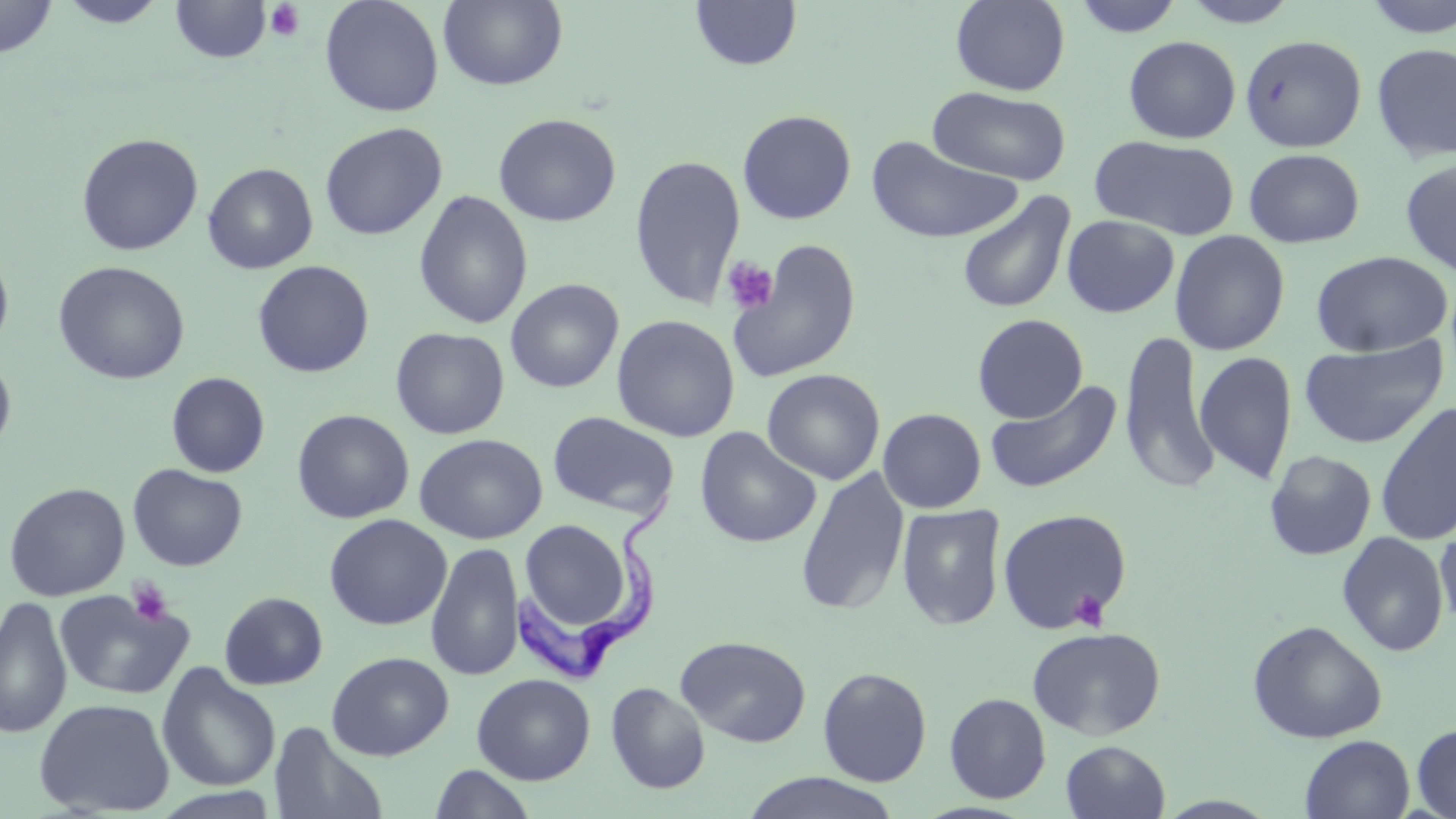 Approximate bounding boxes as named x1/y1/x2/y2 corners in pixels. Platelet locations: (x1=265, y1=2, x2=306, y2=43), (x1=721, y1=257, x2=780, y2=315), (x1=127, y1=578, x2=175, y2=627), (x1=1071, y1=590, x2=1109, y2=630). Trypanosoma brucei locations: (x1=513, y1=489, x2=677, y2=692). Uninfected red blood cell locations: (x1=0, y1=0, x2=57, y2=58), (x1=57, y1=0, x2=169, y2=28), (x1=320, y1=0, x2=444, y2=117), (x1=438, y1=0, x2=568, y2=90), (x1=689, y1=0, x2=803, y2=72), (x1=950, y1=0, x2=1071, y2=95), (x1=1069, y1=0, x2=1185, y2=39), (x1=1180, y1=0, x2=1302, y2=28), (x1=1359, y1=0, x2=1456, y2=40), (x1=170, y1=1, x2=272, y2=64), (x1=1239, y1=34, x2=1367, y2=153), (x1=1123, y1=35, x2=1241, y2=144), (x1=1371, y1=42, x2=1456, y2=163), (x1=927, y1=86, x2=1072, y2=185), (x1=737, y1=110, x2=856, y2=224), (x1=493, y1=113, x2=621, y2=227), (x1=319, y1=122, x2=448, y2=241), (x1=75, y1=132, x2=204, y2=256), (x1=1089, y1=134, x2=1241, y2=240), (x1=866, y1=135, x2=1022, y2=245), (x1=1243, y1=148, x2=1366, y2=248), (x1=629, y1=154, x2=747, y2=311), (x1=1399, y1=157, x2=1456, y2=278), (x1=203, y1=162, x2=318, y2=274), (x1=413, y1=190, x2=534, y2=330), (x1=956, y1=190, x2=1076, y2=314), (x1=1061, y1=215, x2=1180, y2=317), (x1=1170, y1=230, x2=1290, y2=355), (x1=725, y1=238, x2=863, y2=383), (x1=0, y1=248, x2=14, y2=357), (x1=1311, y1=250, x2=1453, y2=356), (x1=252, y1=260, x2=374, y2=378), (x1=53, y1=261, x2=190, y2=384), (x1=505, y1=279, x2=624, y2=393), (x1=972, y1=313, x2=1088, y2=423), (x1=611, y1=315, x2=740, y2=441), (x1=390, y1=327, x2=510, y2=439), (x1=1118, y1=329, x2=1221, y2=495), (x1=1298, y1=337, x2=1449, y2=450), (x1=1194, y1=350, x2=1298, y2=485), (x1=0, y1=353, x2=16, y2=457), (x1=762, y1=369, x2=885, y2=484), (x1=166, y1=372, x2=270, y2=477), (x1=984, y1=379, x2=1123, y2=495), (x1=1375, y1=400, x2=1456, y2=546), (x1=877, y1=408, x2=987, y2=513), (x1=292, y1=409, x2=414, y2=523), (x1=547, y1=411, x2=680, y2=520), (x1=694, y1=427, x2=822, y2=548), (x1=414, y1=433, x2=548, y2=544), (x1=1264, y1=450, x2=1377, y2=560), (x1=128, y1=464, x2=247, y2=571), (x1=796, y1=467, x2=910, y2=617), (x1=4, y1=481, x2=130, y2=602), (x1=896, y1=503, x2=1007, y2=631), (x1=997, y1=508, x2=1132, y2=635), (x1=324, y1=513, x2=451, y2=630), (x1=517, y1=518, x2=637, y2=640), (x1=1435, y1=519, x2=1456, y2=635), (x1=1336, y1=531, x2=1450, y2=656), (x1=426, y1=541, x2=525, y2=681), (x1=54, y1=588, x2=195, y2=700), (x1=219, y1=591, x2=328, y2=690), (x1=0, y1=595, x2=72, y2=739), (x1=1248, y1=620, x2=1387, y2=743), (x1=1027, y1=625, x2=1165, y2=739), (x1=676, y1=635, x2=812, y2=747), (x1=326, y1=651, x2=454, y2=761), (x1=157, y1=663, x2=281, y2=792), (x1=818, y1=666, x2=932, y2=786), (x1=472, y1=673, x2=596, y2=784), (x1=605, y1=681, x2=711, y2=794), (x1=944, y1=692, x2=1051, y2=804), (x1=34, y1=697, x2=176, y2=816), (x1=269, y1=722, x2=387, y2=819), (x1=1412, y1=723, x2=1456, y2=818), (x1=1300, y1=735, x2=1415, y2=818), (x1=1060, y1=740, x2=1170, y2=819), (x1=428, y1=765, x2=538, y2=819), (x1=739, y1=772, x2=904, y2=819). Slide-level diagnosis: Trypanosoma brucei. Light microscopy. 1000x magnification. Image is 1456×819 pixels. Thin blood film. Single field of view. May-Grünwald-Giemsa stain.